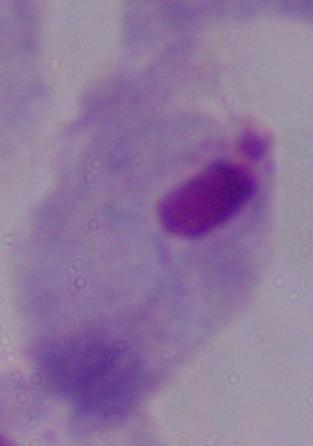
Captured at 1000x magnification. A trichomonad is shown. Photomicrograph.